Identify the cell.
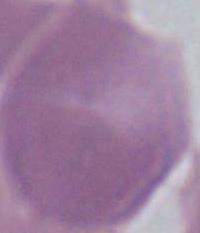
An erythrocyte.

{
  "modality": "photomicrograph",
  "magnification": "1000x"
}